Classify this cell by malaria status.
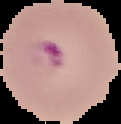
Parasitized.

Summary:
  - Image size: 121×124 pixels
  - Image type: cell region segmented out of the field of view; surrounding area masked to black
  - Preparation: thin blood smear